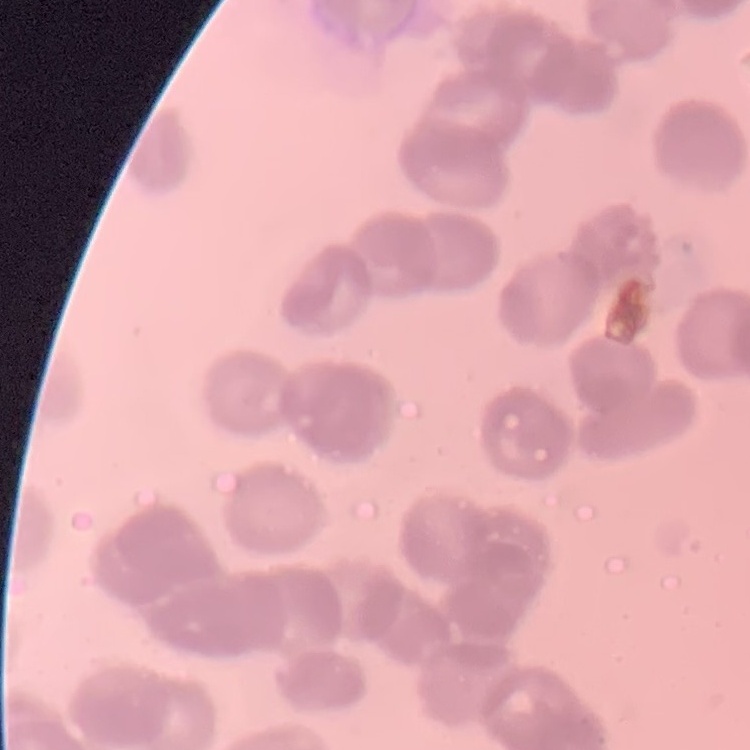 The red blood cells exhibit rouleaux formation. Thin blood film. Field's or Giemsa stain. Square crop of a larger photomicrograph.